Classify this cell by malaria status.
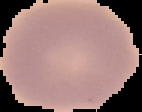
Uninfected.

Segmented cell region on a black background. Image is 142×112 pixels. From a thin blood film.